Identify the parasite.
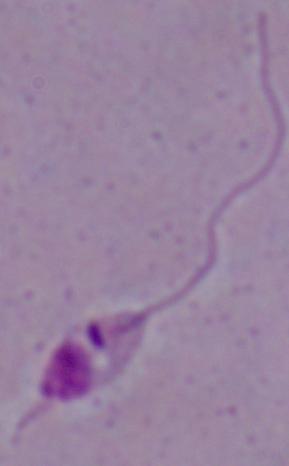

This is Leishmania.

Photomicrograph. 1000x magnification.